Name the blood parasite species.
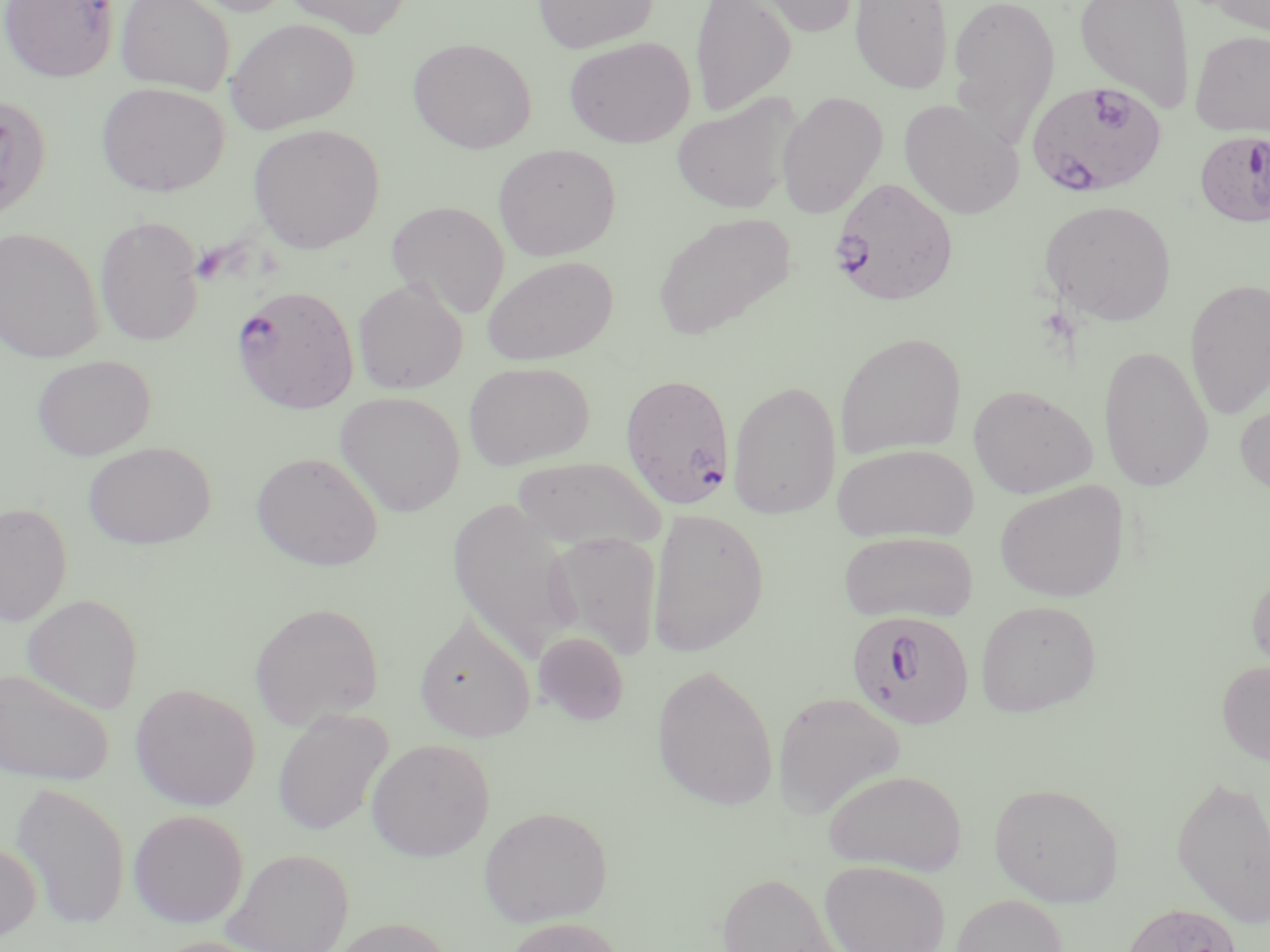

Plasmodium falciparum.

Approximate bounding boxes as [x1, y1, x2, y2] in pixels. Uninfected red blood cell locations: [115, 0, 234, 95], [183, 0, 298, 16], [282, 0, 413, 37], [533, 0, 658, 53], [690, 0, 796, 118], [742, 0, 861, 37], [850, 0, 954, 95], [947, 0, 1061, 144], [1074, 0, 1195, 113], [1201, 0, 1270, 35], [226, 18, 360, 134], [1190, 30, 1270, 136], [408, 37, 537, 153], [565, 37, 696, 147], [96, 82, 229, 196], [776, 92, 888, 219], [0, 94, 52, 221], [671, 94, 800, 215], [898, 99, 1024, 219], [247, 123, 385, 252], [492, 144, 621, 261], [386, 200, 510, 319], [1039, 200, 1176, 326], [653, 212, 796, 339], [94, 215, 204, 347], [0, 226, 104, 363], [482, 255, 618, 366], [352, 278, 468, 394], [1184, 278, 1270, 420], [834, 332, 966, 460], [1098, 345, 1214, 492], [33, 355, 155, 460], [463, 361, 595, 470], [727, 379, 842, 520], [968, 384, 1097, 499], [335, 390, 466, 516], [1234, 398, 1270, 501], [83, 441, 216, 549], [833, 442, 978, 543], [251, 451, 383, 571], [512, 456, 668, 552], [995, 480, 1130, 602], [447, 498, 578, 661], [0, 503, 72, 626], [647, 508, 769, 658], [838, 531, 978, 624], [544, 532, 663, 661], [1247, 565, 1270, 678], [21, 593, 144, 713], [975, 599, 1102, 717], [250, 601, 384, 729], [415, 612, 536, 742], [534, 630, 630, 725], [1216, 659, 1270, 765], [652, 663, 779, 811], [0, 667, 114, 786], [129, 682, 261, 811], [772, 691, 906, 819], [272, 708, 393, 836], [366, 737, 495, 861], [824, 768, 968, 875], [1171, 774, 1270, 929], [9, 780, 131, 930], [988, 782, 1124, 907], [478, 805, 613, 926], [128, 808, 249, 928], [0, 839, 41, 944], [221, 848, 354, 952], [818, 860, 950, 952], [716, 871, 849, 952], [951, 894, 1068, 952], [1119, 901, 1244, 952], [503, 916, 629, 952], [325, 917, 458, 952], [148, 936, 277, 952]. Plasmodium falciparum-infected red blood cell locations: [0, 0, 119, 82], [1026, 81, 1168, 198], [1194, 130, 1270, 227], [829, 176, 957, 305], [231, 284, 359, 413], [620, 372, 735, 509], [846, 610, 975, 730]. Image is 1270×952 pixels. Captured at 1000x magnification. Thin blood smear. One field of a larger specimen. Light microscopy. May-Grünwald-Giemsa stain.